Assess this cell for malaria.
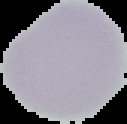

Uninfected.

Summary:
  - Image size: 127×124 pixels
  - Image type: segmented cell region with the area outside set to black
  - Preparation: thin blood smear